Give the position of every Plasmodium parasite.
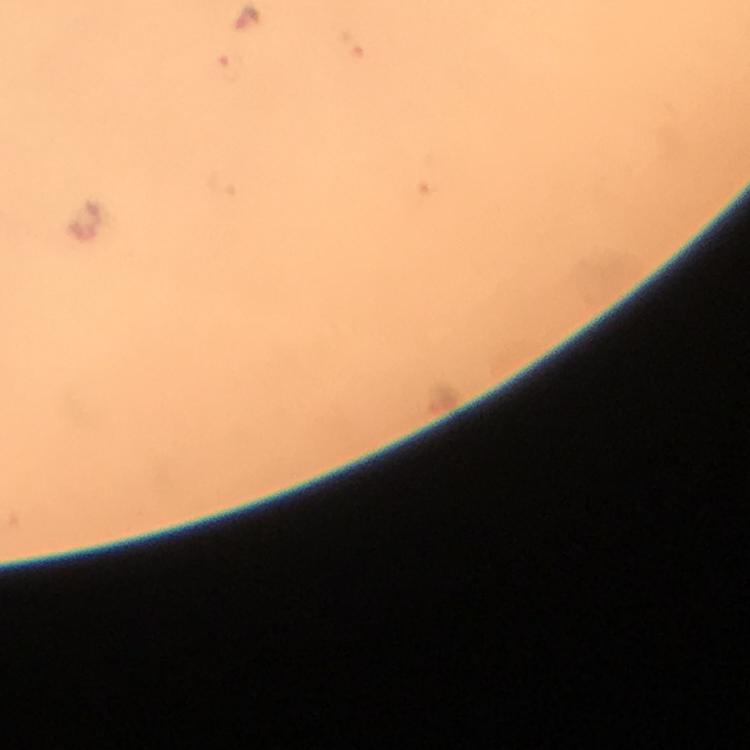

Approximate centers as (x, y) in pixels.
Plasmodium parasites: (247, 19).

Photographed with a smartphone mounted on the microscope. Thick blood film. Image is 750×750 pixels. Immersion oil was used. 100x magnification. Cropped region of a single field of view. Giemsa stain. From a malaria diagnostic workup.